Locate every Plasmodium falciparum-infected red blood cell.
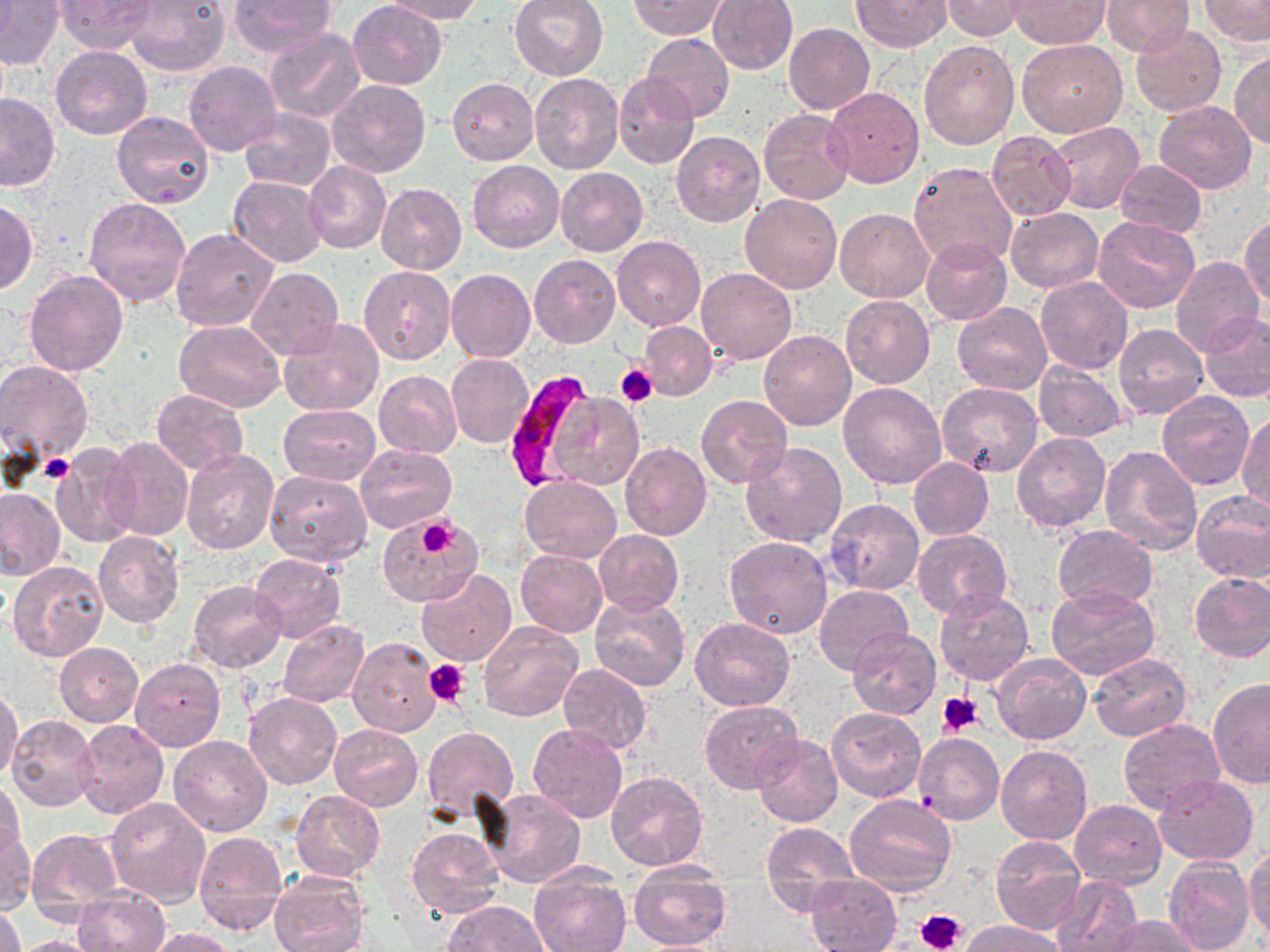

Approximate bounding boxes as (x1,y1)-(x2,y2) corner pairs in pixels.
Plasmodium falciparum-infected red blood cells: (500,371)-(599,492).

Summary:
  - Platelet locations: (615,362)-(659,405), (40,455)-(73,483), (416,517)-(456,557), (425,658)-(470,706), (938,691)-(983,736), (916,908)-(966,951)
  - Uninfected red blood cell locations: (54,0)-(156,54), (126,0)-(232,75), (227,0)-(337,56), (349,0)-(447,88), (384,0)-(485,23), (509,0)-(610,80), (707,0)-(799,74), (852,0)-(950,51), (1007,0)-(1111,49), (1100,0)-(1193,56), (1199,0)-(1269,46), (0,1)-(65,70), (630,1)-(729,40), (942,1)-(1031,40), (784,22)-(875,114), (1131,23)-(1226,117), (263,27)-(365,125), (642,32)-(734,123), (1017,38)-(1127,137), (918,40)-(1019,150), (51,45)-(152,139), (1230,51)-(1270,149), (184,59)-(281,156), (613,71)-(700,168), (530,72)-(623,174), (447,77)-(539,166), (326,79)-(431,178), (824,87)-(924,189), (0,93)-(60,192), (1153,100)-(1257,193), (235,108)-(335,191), (757,108)-(855,204), (112,112)-(215,209), (1049,122)-(1144,215), (987,130)-(1076,220), (672,132)-(765,228), (468,160)-(563,252), (1115,160)-(1207,237), (303,162)-(391,253), (909,162)-(1018,269), (555,167)-(648,256), (228,175)-(328,267), (376,182)-(468,275), (83,194)-(191,307), (740,194)-(841,294), (0,197)-(38,296), (1006,208)-(1103,292), (834,209)-(933,303), (1240,215)-(1269,311), (1093,216)-(1201,315), (170,227)-(277,333), (612,235)-(706,331), (920,237)-(1013,325), (529,255)-(620,348), (1170,256)-(1265,357), (358,264)-(455,366), (245,266)-(344,360), (696,268)-(797,364), (445,269)-(535,362), (24,270)-(128,375), (1036,277)-(1132,375), (839,296)-(934,388), (953,303)-(1052,395), (1200,312)-(1270,404), (279,319)-(383,417), (175,320)-(285,413), (640,321)-(717,399), (1115,323)-(1210,421), (759,330)-(856,430), (446,353)-(533,449), (0,362)-(93,461), (1034,362)-(1128,442), (374,371)-(462,459), (838,382)-(947,489), (937,383)-(1044,478), (152,390)-(248,474), (550,391)-(646,491), (1156,392)-(1254,490), (696,395)-(792,487), (279,405)-(381,485), (1237,411)-(1269,513), (1012,432)-(1109,532), (103,436)-(193,541), (355,442)-(458,532), (620,442)-(712,541), (740,442)-(847,548), (51,445)-(142,548), (1100,445)-(1201,556), (181,449)-(278,554), (908,457)-(993,540), (264,470)-(373,566), (519,477)-(621,563), (0,486)-(66,582), (1191,491)-(1270,584), (824,499)-(925,596), (376,516)-(478,605), (1053,525)-(1157,609), (594,530)-(684,615), (93,531)-(184,627), (913,531)-(1011,620), (725,536)-(833,639), (515,549)-(607,637), (248,553)-(346,643), (8,560)-(108,661), (416,568)-(517,665), (1188,570)-(1270,662), (188,580)-(287,673), (814,584)-(913,676), (1046,584)-(1159,679), (934,588)-(1034,686), (590,593)-(690,690), (689,617)-(795,709), (277,619)-(370,708), (478,622)-(582,722), (847,627)-(940,721), (349,638)-(439,736), (55,642)-(143,727), (992,654)-(1091,746), (1087,654)-(1190,741), (131,658)-(226,752), (558,664)-(652,754), (1207,677)-(1270,789), (0,687)-(22,785), (244,692)-(341,789), (699,700)-(805,794), (827,707)-(928,803), (6,716)-(100,813), (74,718)-(169,819), (1117,718)-(1225,814), (527,723)-(628,823), (329,724)-(423,811), (422,726)-(519,819), (914,732)-(1004,824), (168,735)-(272,837), (752,735)-(843,828), (995,745)-(1092,846), (606,771)-(708,870), (0,776)-(25,862), (1152,776)-(1258,866), (483,788)-(586,888), (291,789)-(385,881), (845,794)-(956,897), (105,796)-(212,906), (1070,800)-(1166,888), (761,822)-(858,913), (2,826)-(35,914), (26,828)-(122,923), (407,828)-(504,919), (194,832)-(289,936), (990,835)-(1085,935), (1244,845)-(1270,943), (1164,858)-(1254,952), (626,861)-(733,951), (528,865)-(632,952), (270,870)-(369,952), (805,874)-(901,951), (1052,874)-(1143,952), (70,887)-(172,952), (441,900)-(550,952), (0,904)-(26,952), (1103,915)-(1203,952), (960,919)-(1067,952), (147,927)-(237,952), (9,935)-(107,952)
  - Slide-level diagnosis: Plasmodium falciparum
  - Stain: May-Grünwald-Giemsa
  - Modality: light microscopy
  - Preparation: thin blood film
  - Magnification: 1000x
  - Image size: 1270×952 pixels
  - Field of view: single